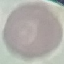

Summary:
  - Result: no malaria parasites seen
  - Preparation: thin blood film
  - Image type: cell patch, automatically extracted from a larger field of view and resized to 64 × 64 pixels
  - Capture: smartphone camera at the microscope eyepiece
  - Stain: Giemsa